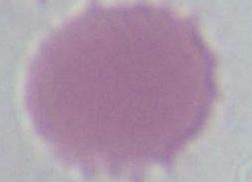

Summary:
  - Modality: micrograph
  - Identification: erythrocyte
  - Magnification: 1000x